Locate every Plasmodium malariae-infected red blood cell.
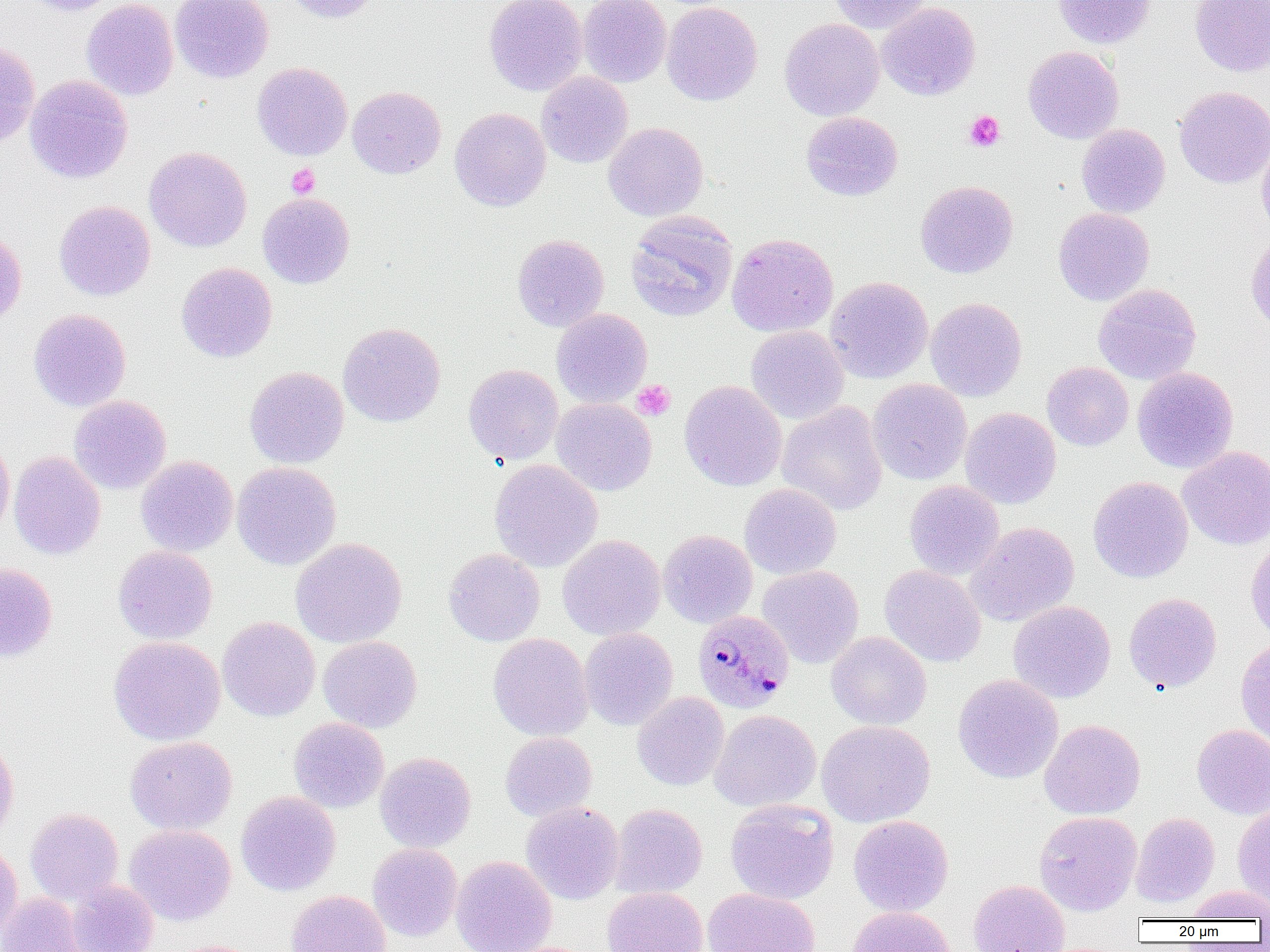

Approximate bounding boxes as (x1, y1, x2, y2) in pixels.
Plasmodium malariae-infected red blood cells: (693, 610, 794, 713).

Summary:
  - Platelet locations: (964, 110, 1005, 152), (286, 163, 320, 198), (632, 380, 675, 420)
  - Uninfected red blood cell locations: (21, 0, 119, 16), (81, 0, 178, 101), (170, 0, 273, 83), (282, 0, 384, 23), (484, 0, 587, 95), (577, 0, 671, 87), (828, 0, 933, 33), (1053, 0, 1155, 48), (1190, 0, 1270, 77), (661, 1, 762, 106), (876, 2, 981, 101), (779, 18, 884, 121), (0, 40, 40, 150), (1023, 46, 1124, 144), (252, 62, 353, 161), (536, 72, 633, 168), (25, 74, 133, 184), (347, 86, 446, 179), (1174, 86, 1270, 188), (449, 107, 551, 211), (801, 111, 902, 201), (603, 122, 708, 222), (1076, 123, 1170, 218), (1257, 134, 1270, 237), (144, 146, 252, 252), (915, 180, 1018, 278), (257, 193, 355, 288), (54, 200, 155, 301), (1053, 207, 1154, 306), (625, 210, 738, 322), (0, 226, 26, 328), (1246, 232, 1270, 335), (726, 233, 838, 337), (512, 234, 609, 332), (176, 262, 277, 362), (825, 276, 933, 383), (1093, 283, 1201, 385), (925, 297, 1027, 401), (551, 308, 653, 407), (28, 309, 131, 411), (338, 322, 445, 426), (745, 325, 849, 425), (1042, 361, 1133, 451), (463, 364, 563, 464), (244, 366, 349, 469), (1133, 367, 1238, 473), (868, 378, 972, 485), (679, 380, 787, 491), (69, 395, 171, 494), (551, 398, 657, 496), (777, 401, 887, 516), (960, 408, 1061, 509), (0, 433, 15, 543), (1178, 446, 1270, 550), (9, 451, 106, 560), (136, 456, 238, 556), (489, 459, 602, 572), (232, 461, 342, 570), (1088, 476, 1193, 583), (904, 480, 1004, 580), (739, 483, 841, 579), (967, 522, 1079, 626), (658, 529, 757, 628), (558, 534, 665, 640), (290, 537, 407, 648), (1246, 537, 1270, 641), (113, 545, 218, 644), (444, 548, 545, 646), (0, 563, 57, 662), (758, 565, 864, 668), (880, 565, 986, 667), (1123, 592, 1222, 693), (1008, 601, 1115, 703), (217, 616, 320, 722), (579, 627, 678, 730), (826, 632, 932, 730), (488, 633, 593, 741), (108, 636, 225, 746), (318, 636, 422, 733), (1236, 638, 1270, 746), (953, 674, 1063, 784), (632, 691, 730, 791), (709, 709, 821, 812), (289, 717, 389, 813), (1039, 719, 1146, 820), (816, 720, 935, 827), (1192, 724, 1270, 819), (500, 732, 597, 821), (0, 735, 19, 841), (125, 736, 237, 835), (375, 752, 476, 852), (236, 791, 341, 896), (725, 798, 839, 905), (521, 801, 624, 904), (609, 803, 707, 899), (1233, 805, 1270, 909), (25, 807, 123, 905), (1034, 811, 1142, 915), (1131, 813, 1220, 907), (848, 815, 953, 916), (124, 824, 236, 925), (0, 840, 23, 939), (367, 843, 463, 941), (451, 856, 556, 952), (968, 879, 1070, 952), (66, 880, 159, 952), (601, 886, 708, 952), (1185, 886, 1270, 922), (703, 888, 820, 952), (287, 889, 390, 952), (0, 892, 89, 952), (847, 906, 956, 952), (162, 939, 262, 952)
  - Slide-level diagnosis: Plasmodium malariae
  - Field of view: one of a larger specimen
  - Magnification: 1000x
  - Modality: optical microscopy
  - Image size: 1270×952 pixels
  - Preparation: thin blood smear